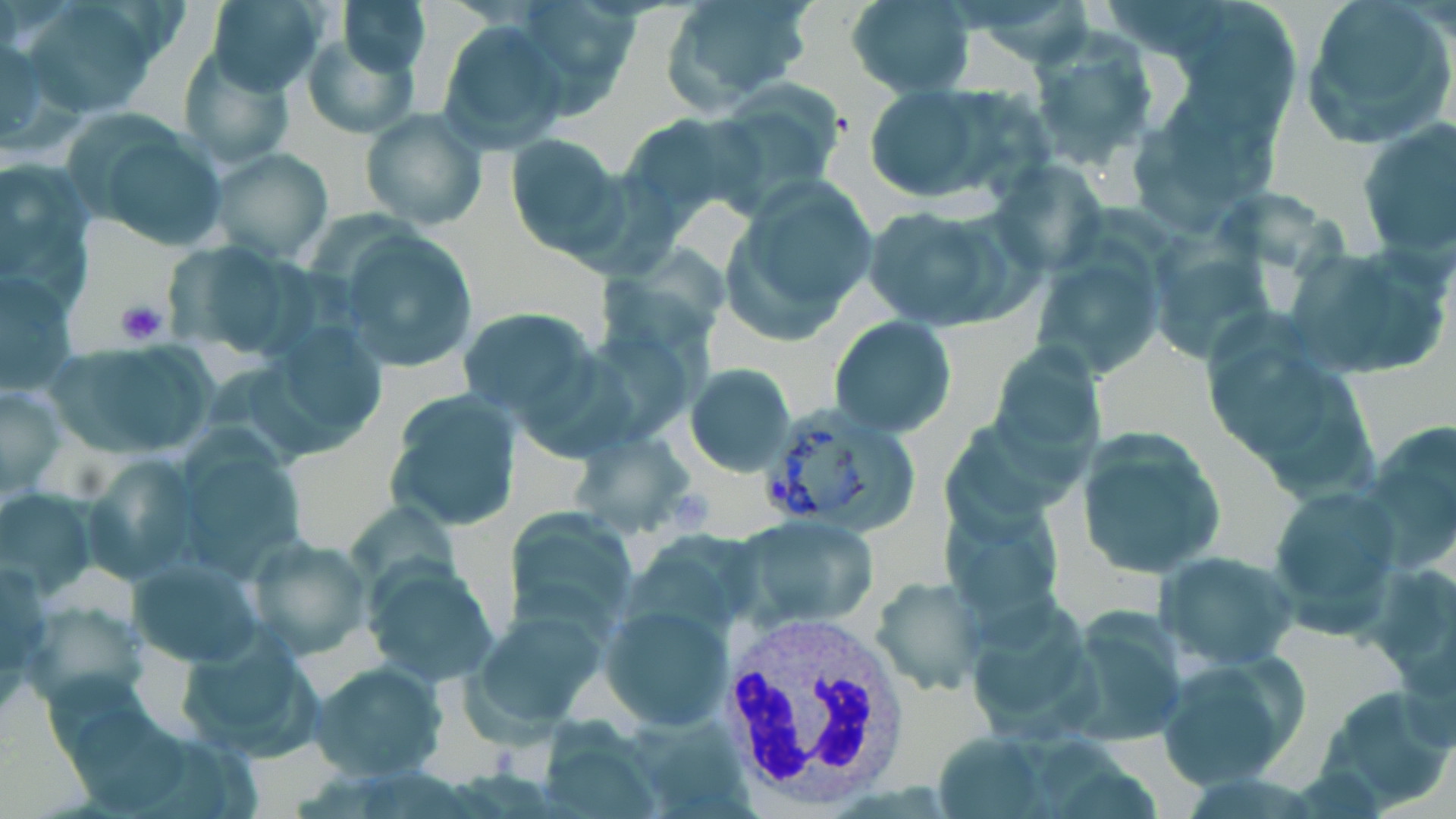
Approximate bounding boxes as [x1, y1, x2, y2] in pixels. Uninfected red blood cell locations: [21, 0, 164, 119], [204, 0, 330, 95], [339, 0, 431, 77], [506, 0, 638, 114], [845, 0, 976, 97], [1299, 0, 1455, 147], [659, 1, 817, 110], [437, 18, 567, 154], [1026, 30, 1164, 177], [1, 32, 49, 147], [301, 34, 418, 141], [175, 49, 295, 169], [709, 84, 847, 209], [862, 87, 996, 199], [359, 108, 488, 232], [618, 111, 756, 222], [1356, 120, 1455, 258], [77, 121, 232, 253], [504, 133, 623, 257], [206, 146, 335, 263], [0, 155, 96, 302], [988, 160, 1105, 275], [729, 176, 879, 328], [863, 203, 1020, 331], [335, 228, 480, 372], [163, 240, 309, 363], [1285, 242, 1451, 381], [1030, 246, 1166, 379], [1, 271, 80, 398], [455, 306, 600, 420], [831, 315, 956, 439], [987, 337, 1104, 474], [44, 341, 222, 460], [685, 362, 795, 476], [0, 383, 66, 496], [383, 389, 524, 533], [1360, 421, 1456, 567], [1075, 428, 1226, 577], [571, 429, 697, 537], [80, 453, 199, 585], [1266, 486, 1405, 634], [0, 487, 98, 597], [507, 508, 639, 635], [736, 514, 880, 628], [249, 536, 372, 660], [1154, 550, 1299, 669], [127, 551, 267, 665], [362, 558, 498, 688], [873, 577, 986, 695], [16, 597, 151, 715], [601, 603, 732, 732], [472, 608, 605, 731], [1056, 609, 1189, 748], [174, 628, 324, 763], [1153, 648, 1304, 790], [309, 662, 447, 781], [1314, 684, 1456, 810]. Platelet locations: [115, 298, 171, 349]. White blood cell locations: [717, 615, 908, 804]. Plasmodium vivax-infected red blood cell locations: [758, 404, 921, 532]. Slide-level diagnosis: Plasmodium vivax. Optical microscopy. Thin blood smear. 1000x magnification. Image is 1456×819 pixels. One field of a larger specimen. May-Grünwald-Giemsa stain.